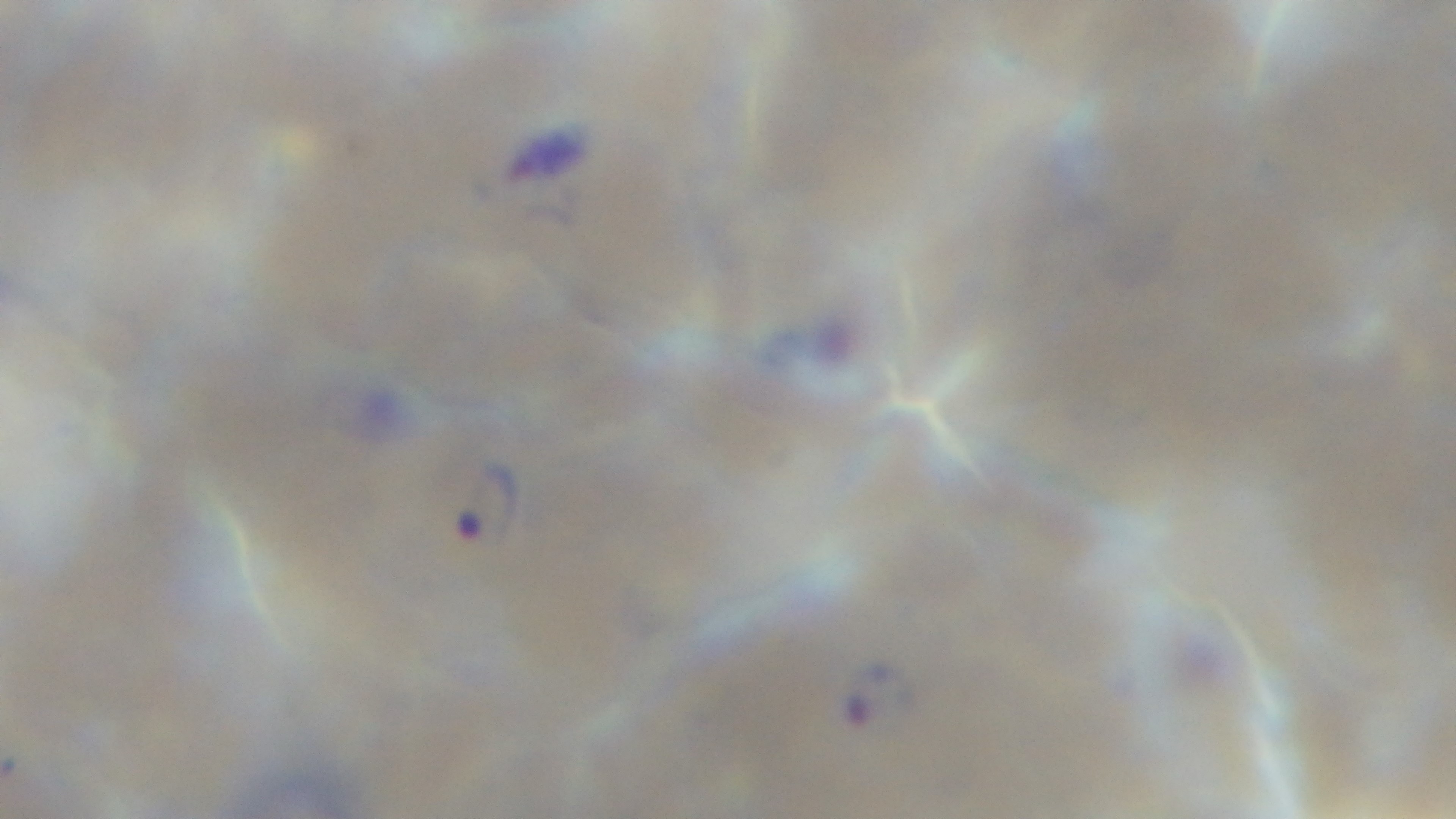
Summary:
  - Modality: light microscopy
  - Objective: 100x oil immersion
  - Stain: Giemsa
  - Field of view: single
  - Capture: mounted 4K digital camera
  - Preparation: thin blood film
  - Malaria status: positive